Assess this cell for malaria.
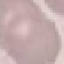

It is uninfected.

Giemsa-stained preparation. Photographed with a smartphone camera at the microscope eyepiece. Thin blood smear. Automatically extracted cell patch, resized to 64 × 64 pixels.